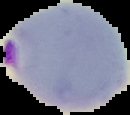
image type = segmented cell region on a black background
preparation = thin blood film
malaria status = parasitized
image size = 130×115 pixels